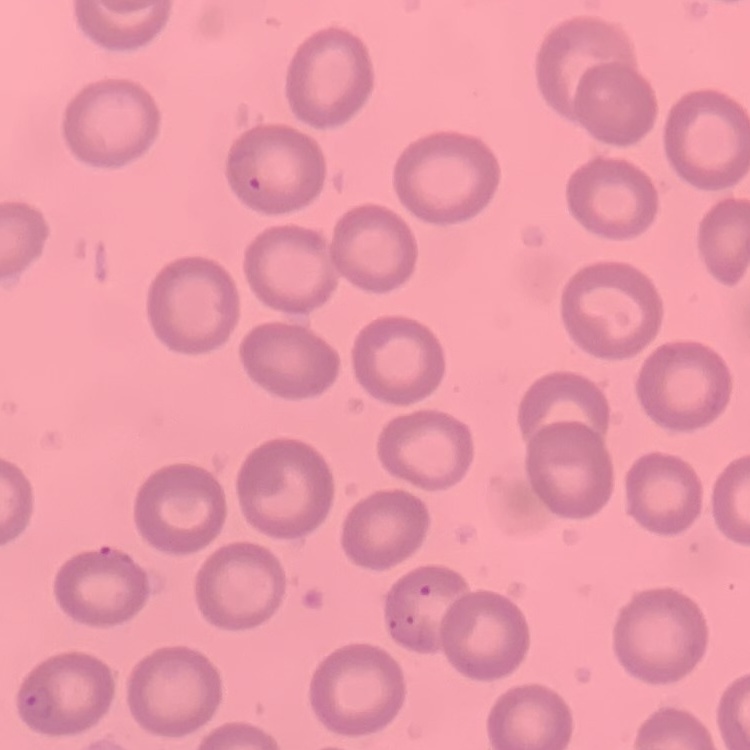

The erythrocytes exhibit no rouleaux formation. Thin peripheral smear. Field's or Giemsa stain. Square crop of a larger photomicrograph.